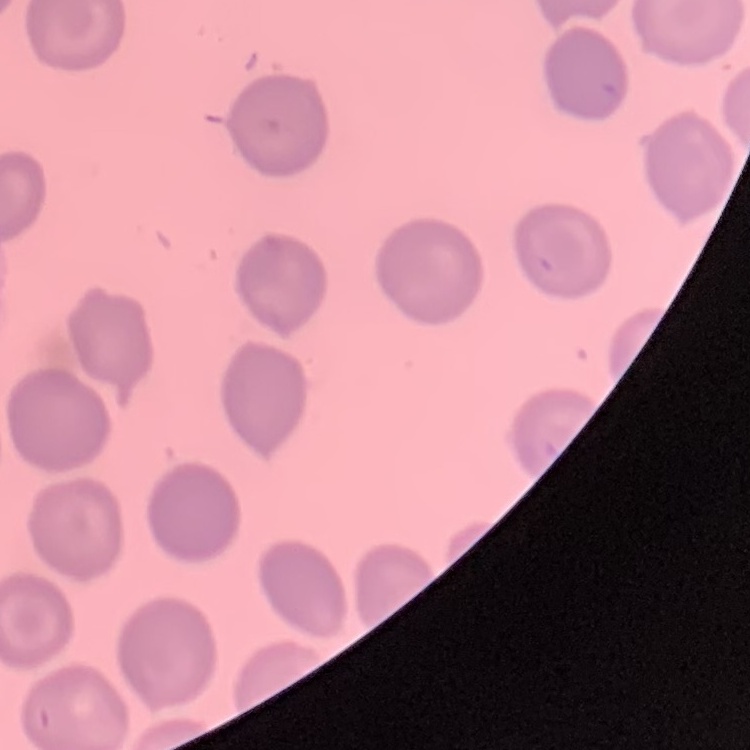

red blood cell morphology = no rouleaux formation
image type = one tile cut from a larger photomicrograph
preparation = thin peripheral smear
stain = Field's or Giemsa